Outline each blood parasite and name the species.
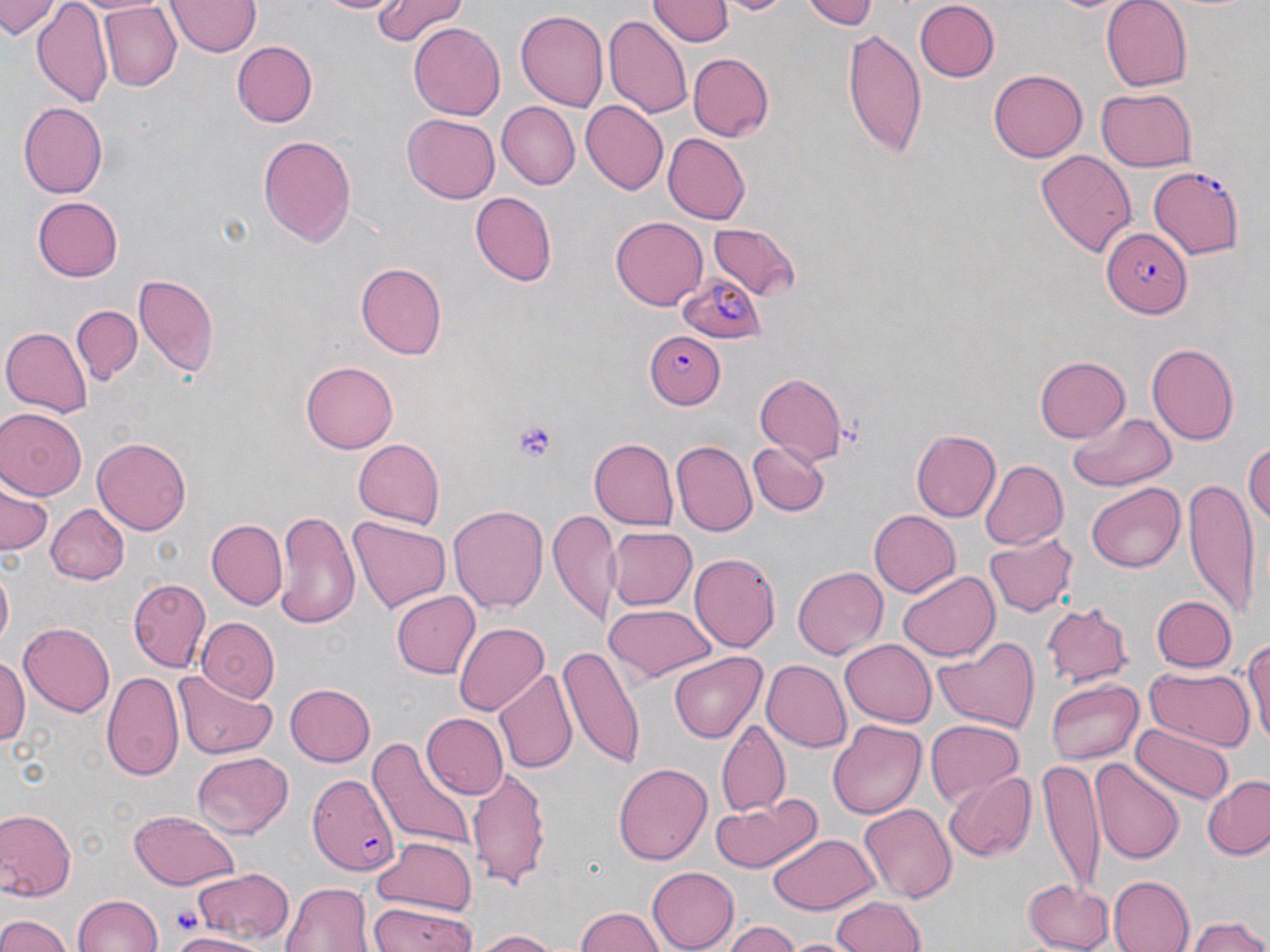
Approximate bounding boxes as (x1, y1, x2, y2) in pixels.
Plasmodium falciparum-infected red blood cells: (1149, 165, 1248, 261), (1100, 226, 1193, 319), (679, 273, 767, 346), (647, 331, 726, 410), (308, 771, 401, 877).
No Plasmodium ovale, Plasmodium malariae, Plasmodium vivax, Babesia divergens, or Trypanosoma brucei observed.

{
  "slide_level_diagnosis": "Plasmodium falciparum",
  "modality": "light microscopy",
  "platelet_locations": "approximate bounding boxes as (x1, y1, x2, y2) in pixels: (513, 420, 558, 459), (172, 904, 200, 936)",
  "field_of_view": "one of a larger specimen",
  "stain": "May-Grünwald-Giemsa",
  "magnification": "1000x",
  "preparation": "thin blood smear",
  "uninfected_red_blood_cell_locations": "approximate bounding boxes as (x1, y1, x2, y2) in pixels: (0, 0, 60, 40), (167, 0, 262, 59), (310, 0, 407, 16), (371, 0, 467, 45), (718, 0, 792, 17), (797, 0, 878, 28), (1100, 0, 1195, 92), (649, 1, 731, 48), (913, 1, 1001, 81), (32, 2, 113, 109), (96, 3, 180, 91), (513, 9, 609, 111), (603, 14, 691, 118), (408, 22, 504, 119), (840, 27, 928, 160), (232, 41, 321, 131), (687, 53, 775, 144), (989, 68, 1087, 162), (1096, 87, 1198, 172), (20, 102, 111, 197), (496, 102, 581, 190), (581, 102, 667, 196), (403, 113, 500, 203), (662, 133, 749, 224), (257, 135, 356, 247), (1037, 150, 1136, 259), (469, 191, 556, 285), (32, 198, 123, 281), (611, 217, 707, 309), (710, 225, 800, 303), (356, 262, 447, 357), (132, 273, 223, 378), (72, 304, 142, 386), (0, 324, 91, 420), (1146, 342, 1240, 443), (1034, 356, 1130, 441), (300, 360, 398, 453), (753, 373, 849, 463), (0, 408, 87, 498), (1070, 411, 1178, 492), (910, 428, 1000, 524), (93, 435, 192, 535), (589, 437, 679, 529), (353, 438, 444, 529), (672, 439, 757, 535), (749, 440, 828, 520), (1245, 441, 1270, 534), (978, 459, 1067, 550), (1183, 479, 1258, 620), (1087, 482, 1185, 573), (0, 486, 51, 557), (449, 503, 549, 614), (47, 505, 130, 584), (273, 508, 359, 627), (868, 508, 960, 595), (549, 510, 618, 626), (351, 517, 450, 612), (205, 519, 288, 612), (608, 526, 698, 611), (984, 534, 1077, 618), (689, 551, 782, 650), (792, 565, 889, 659), (1, 569, 13, 650), (896, 571, 999, 662), (130, 578, 210, 670), (390, 590, 479, 679), (1152, 595, 1237, 673), (1040, 601, 1134, 687), (603, 605, 715, 682), (195, 617, 280, 700), (453, 619, 549, 713), (19, 622, 116, 715), (931, 635, 1041, 732), (1243, 635, 1270, 740), (841, 640, 938, 727), (559, 645, 647, 768), (668, 651, 767, 742), (0, 656, 28, 748), (761, 659, 851, 752), (494, 667, 577, 776), (101, 669, 183, 780), (1144, 669, 1250, 750), (174, 671, 278, 759), (1047, 678, 1145, 765), (285, 683, 376, 767), (421, 713, 509, 800), (925, 718, 1027, 805), (828, 719, 926, 819), (715, 720, 790, 815), (1130, 722, 1234, 806), (367, 735, 475, 851), (193, 751, 294, 838), (1091, 758, 1184, 865), (1039, 761, 1105, 894), (613, 762, 712, 865), (465, 768, 554, 890), (942, 771, 1037, 862), (1201, 775, 1270, 860), (714, 792, 820, 871), (858, 802, 957, 903), (129, 809, 238, 889), (1, 810, 75, 899), (766, 832, 881, 913), (371, 835, 479, 918), (646, 866, 740, 950), (191, 867, 295, 943), (1025, 874, 1114, 949), (1106, 875, 1195, 952), (282, 881, 371, 952), (74, 893, 162, 952), (829, 895, 926, 952), (366, 901, 474, 952), (573, 907, 667, 952), (0, 912, 72, 952), (1188, 916, 1270, 952), (721, 920, 798, 952), (471, 929, 565, 951), (166, 931, 262, 952), (787, 936, 857, 952)",
  "image_size": "1270×952 pixels"
}